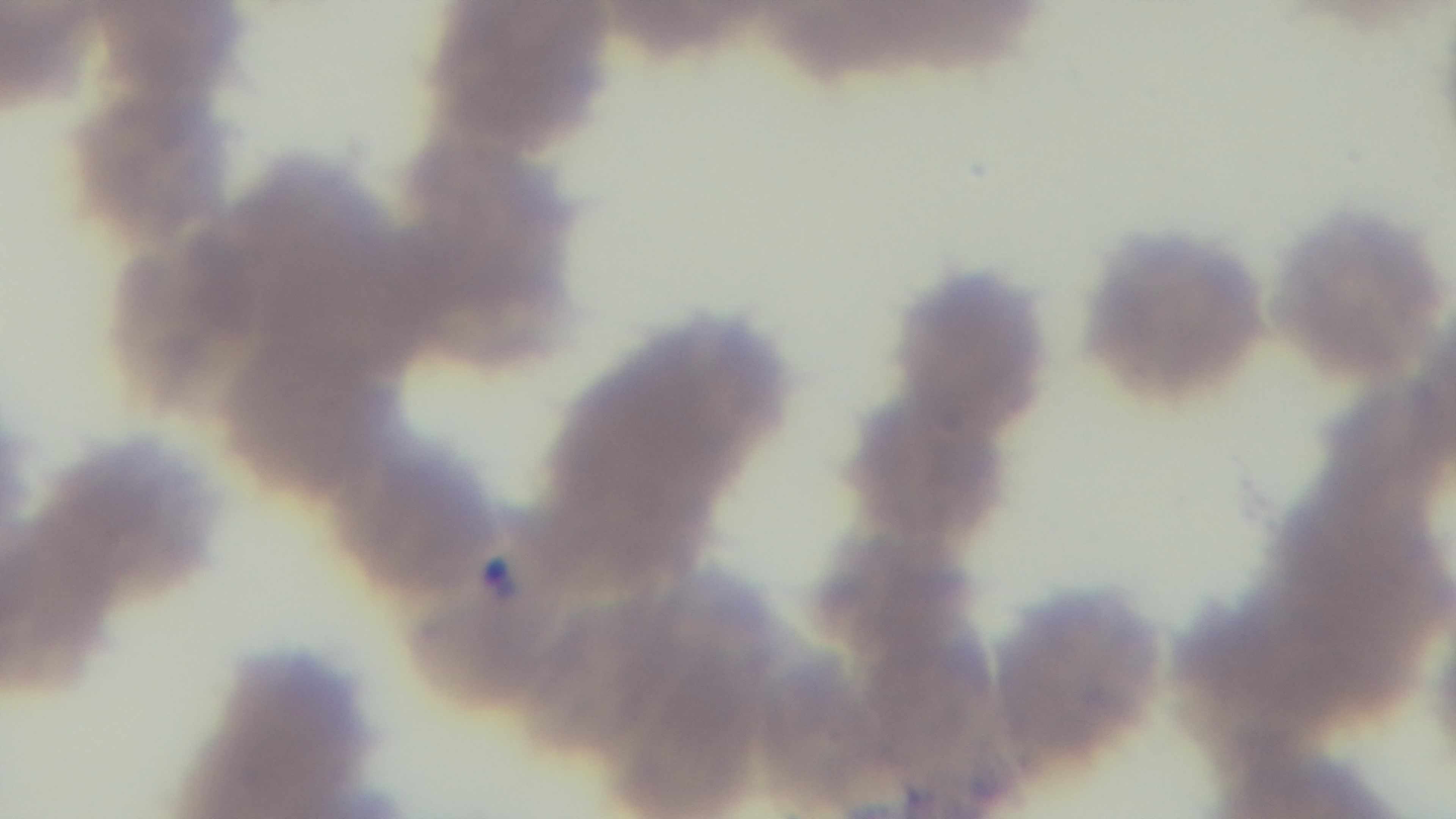
One field from the slide. Preparation: thin blood film. Photomicrograph. Giemsa-stained. Malaria status: infected. Oil-immersion objective, 100x. Captured with a mounted 4K digital camera.